Report the malaria status of this cell.
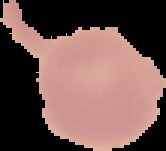
It is uninfected.

Summary:
  - Preparation: thin blood smear
  - Image size: 166×151 pixels
  - Image type: cell region segmented out of the field of view; surrounding area masked to black